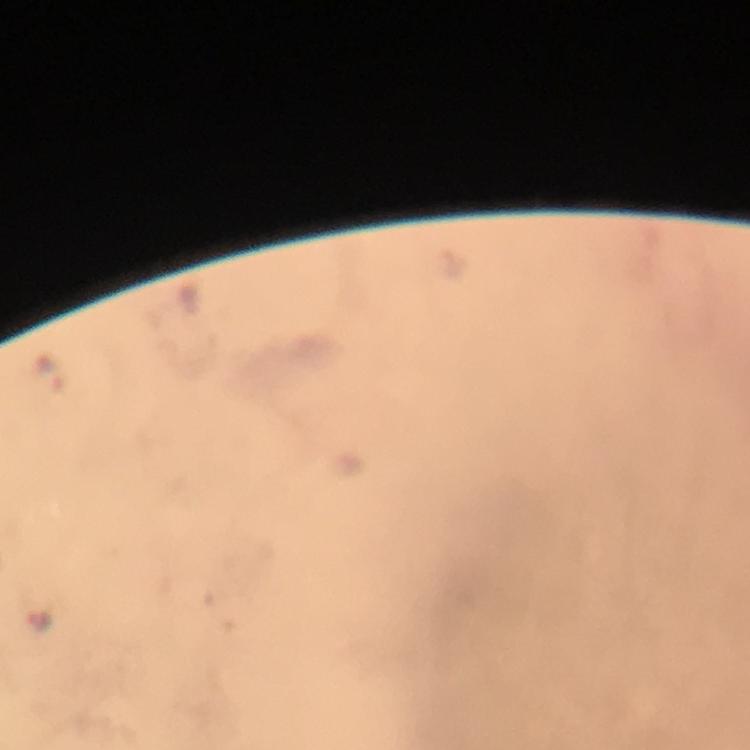
Approximate centers as {x, y} in pixels. Malaria parasite locations: {37, 619}. Giemsa stain. Photographed through the microscope with a smartphone camera. From a diagnostic examination for malaria. Cropped region of a single field of view. Thick blood smear. Image is 750×750 pixels. At 100x magnification. Immersion oil was used.